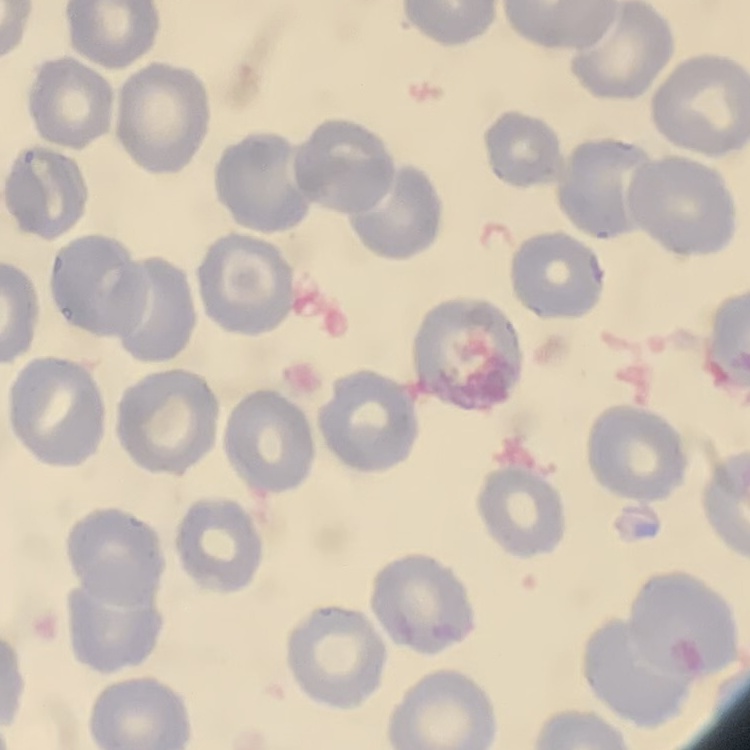

Summary:
  - Erythrocyte morphology: no rouleaux formation
  - Stain: Field's or Giemsa
  - Preparation: thin blood smear
  - Image type: square crop of a larger photomicrograph